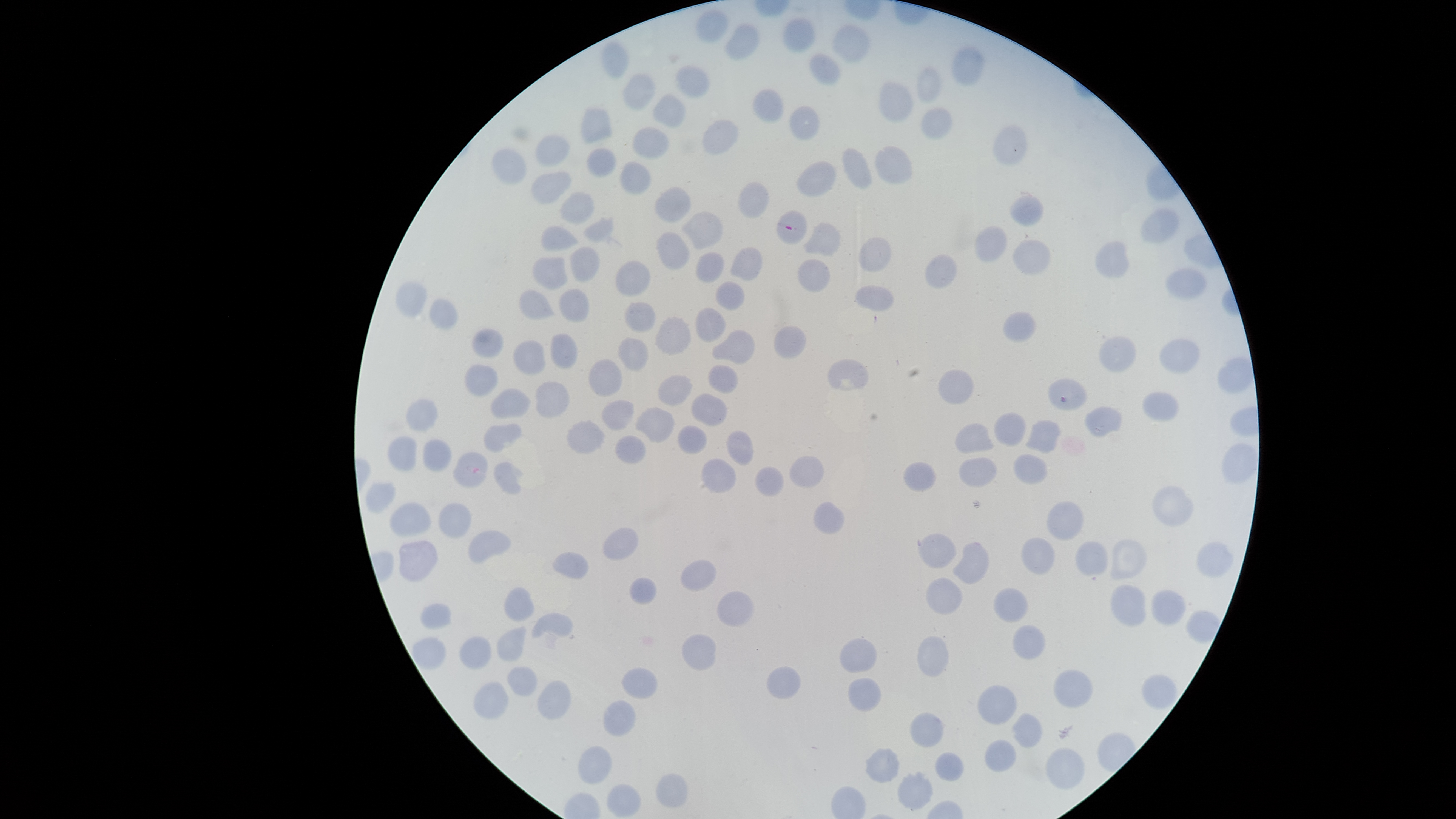

visible region = circular
presence = malaria parasites identified
field of view = single
parasitized red blood cells = approximate bounding boxes as (left, top, right, bottom) in pixels: (776, 210, 808, 245), (1047, 377, 1087, 411)
uninfected red blood cells = approximate bounding boxes as (left, top, right, bottom) in pixels: (695, 9, 728, 43), (782, 16, 815, 53), (723, 23, 759, 61), (832, 23, 871, 63), (601, 40, 629, 80), (951, 46, 985, 85), (809, 53, 840, 84), (674, 65, 710, 98), (916, 67, 944, 104), (621, 72, 655, 110), (878, 80, 913, 123), (752, 89, 784, 123), (652, 93, 686, 127), (789, 106, 819, 140), (920, 106, 953, 140), (580, 107, 612, 145), (702, 119, 738, 155), (993, 124, 1027, 166), (632, 127, 669, 159), (534, 134, 570, 167), (873, 145, 914, 185), (586, 146, 617, 179), (842, 147, 872, 189), (491, 148, 527, 184), (620, 160, 651, 196), (797, 161, 836, 197), (529, 170, 571, 204), (738, 181, 771, 219), (653, 186, 691, 223), (559, 191, 595, 225), (1009, 193, 1044, 227), (1140, 207, 1180, 244), (679, 210, 723, 249), (583, 214, 623, 247), (803, 221, 841, 257), (541, 225, 579, 252), (973, 225, 1008, 262), (655, 232, 691, 271), (857, 237, 892, 272), (1011, 240, 1050, 276), (1094, 240, 1130, 279), (569, 245, 601, 282), (730, 245, 763, 281), (695, 251, 725, 283), (924, 253, 957, 288), (531, 257, 569, 289), (797, 258, 830, 293), (614, 260, 651, 297), (1164, 267, 1208, 299), (714, 280, 745, 310), (395, 281, 429, 317), (855, 285, 894, 311), (518, 288, 557, 319), (558, 288, 590, 322), (428, 298, 459, 329), (624, 301, 657, 332), (695, 306, 727, 343), (1003, 311, 1036, 342), (654, 315, 691, 355), (774, 324, 808, 359), (471, 328, 504, 358), (711, 329, 756, 365), (551, 333, 578, 369), (1098, 335, 1137, 373), (617, 337, 648, 372), (1158, 338, 1199, 375), (513, 340, 547, 375), (587, 358, 623, 397), (827, 358, 869, 391), (464, 364, 498, 397), (707, 364, 738, 393), (938, 368, 974, 405), (657, 374, 693, 406), (534, 380, 571, 419), (489, 388, 533, 418), (1141, 390, 1180, 422), (690, 392, 727, 426), (406, 398, 440, 432), (600, 399, 635, 431), (1083, 405, 1124, 437), (634, 406, 675, 443), (993, 411, 1026, 446), (566, 419, 605, 454), (1025, 420, 1062, 454), (483, 423, 523, 453), (955, 423, 995, 453), (677, 425, 707, 454), (726, 429, 755, 466), (614, 435, 648, 465), (388, 436, 417, 472), (422, 438, 452, 473), (1221, 443, 1257, 485), (1013, 453, 1049, 485), (789, 455, 824, 487), (700, 457, 737, 494), (959, 457, 998, 488), (493, 461, 524, 495), (902, 461, 937, 493), (754, 466, 785, 498), (365, 482, 396, 513), (1151, 486, 1194, 526), (390, 501, 432, 537), (1046, 501, 1084, 541), (437, 502, 472, 538), (813, 502, 845, 534), (602, 527, 639, 560), (468, 530, 511, 563), (917, 531, 957, 569), (1020, 537, 1055, 574), (1110, 538, 1147, 580), (398, 540, 438, 583), (1075, 540, 1108, 575), (952, 541, 989, 584), (1195, 541, 1234, 579), (551, 551, 590, 580), (680, 559, 716, 593), (629, 575, 657, 605), (925, 577, 964, 615), (1110, 584, 1147, 627), (504, 586, 535, 621), (993, 586, 1028, 623), (1151, 589, 1186, 625), (716, 591, 754, 628), (419, 603, 453, 630), (530, 613, 573, 639), (1012, 624, 1046, 660), (497, 626, 527, 662), (681, 633, 717, 671), (917, 635, 949, 677), (458, 636, 493, 670), (838, 636, 878, 673), (411, 637, 447, 672), (507, 666, 538, 697), (766, 666, 801, 700), (621, 667, 658, 700), (1053, 670, 1093, 708), (1140, 674, 1178, 711), (847, 676, 881, 712), (536, 679, 572, 720), (473, 680, 509, 719), (976, 685, 1017, 725), (602, 700, 636, 738), (909, 711, 943, 749), (1010, 712, 1042, 748), (985, 739, 1016, 772), (577, 745, 613, 786), (865, 747, 900, 783), (1046, 747, 1085, 789), (935, 751, 963, 781), (897, 771, 933, 810), (656, 773, 688, 808), (606, 784, 641, 817)
image size = 1456×819 pixels
species = Plasmodium falciparum
capture = smartphone photograph through the microscope eyepiece
stain = Giemsa
preparation = thin blood film